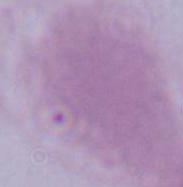 Photomicrograph. 1000x magnification. A red blood cell is seen.